Name the parasite shown.
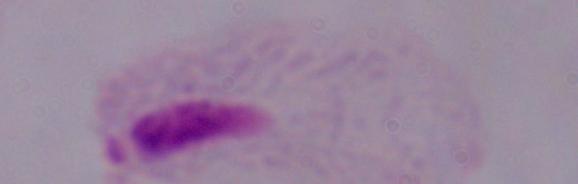

This is a trichomonad.

Summary:
  - Magnification: 1000x
  - Modality: micrograph